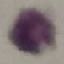
{
  "malaria_status": "uninfected",
  "capture": "smartphone through the microscope eyepiece",
  "image_type": "automatically extracted cell patch, resized to 64 × 64 pixels",
  "preparation": "thin blood smear",
  "stain": "Giemsa"
}